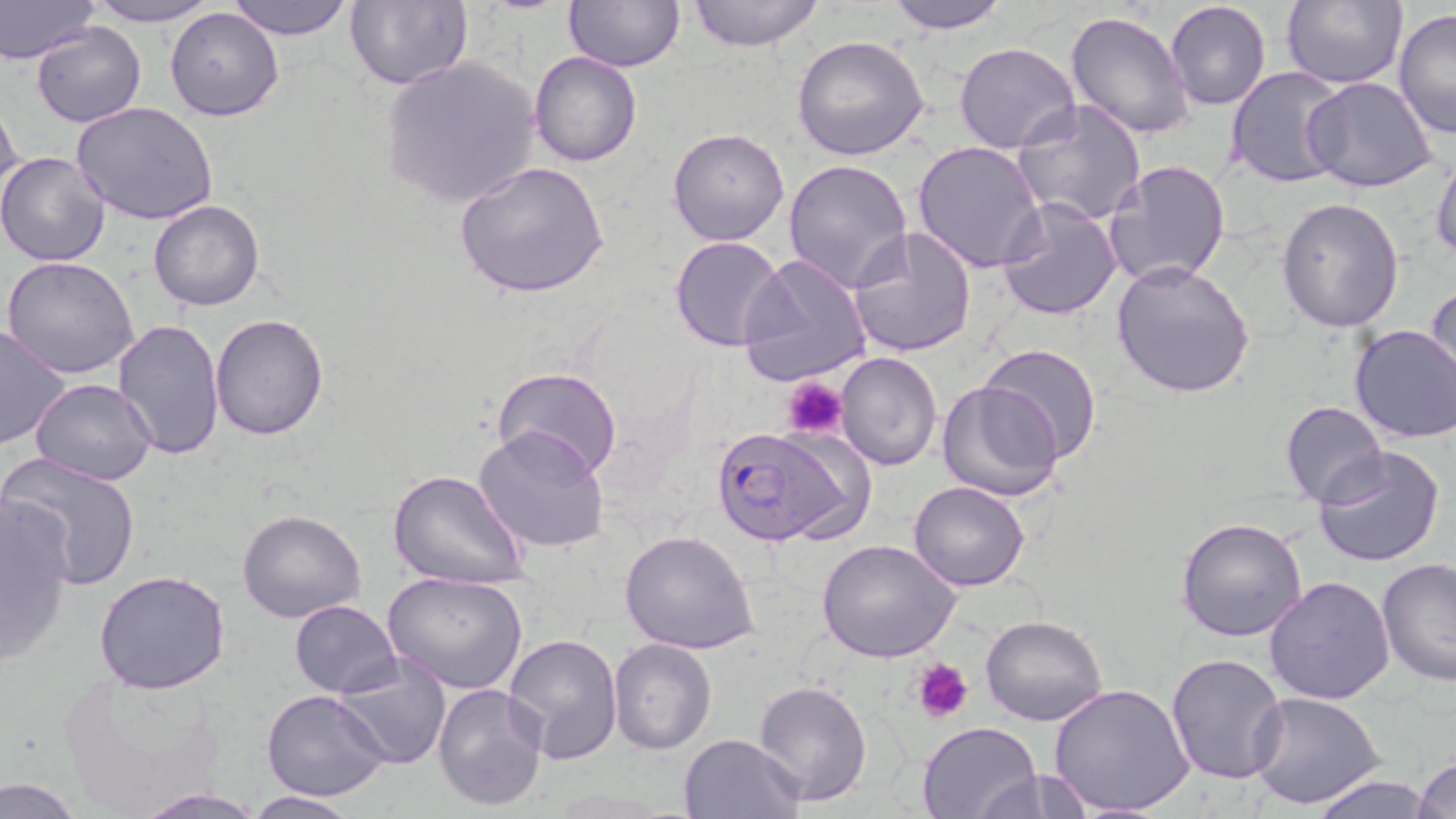

slide_level_diagnosis: Plasmodium falciparum
field_of_view: one of a larger specimen
stain: May-Grünwald-Giemsa
preparation: thin blood film
uninfected_red_blood_cell_locations: 'approximate bounding boxes as (x1,y1)-(x2,y2) corner pairs in pixels: (0,0)-(100,65), (81,0)-(224,26), (227,0)-(355,41), (347,0)-(473,90), (687,0)-(824,51), (886,0)-(1011,33), (1280,0)-(1407,91), (565,1)-(685,71), (1165,1)-(1271,110), (1393,7)-(1456,141), (165,8)-(284,122), (1065,9)-(1196,141), (32,23)-(147,127), (791,35)-(930,160), (952,41)-(1081,153), (530,52)-(643,167), (379,58)-(540,208), (1225,67)-(1350,188), (1302,76)-(1438,193), (0,94)-(23,208), (1013,100)-(1147,226), (73,102)-(221,225), (666,127)-(790,247), (913,139)-(1045,272), (0,150)-(111,268), (1431,150)-(1456,263), (783,156)-(914,293), (1103,158)-(1232,289), (452,161)-(610,299), (996,195)-(1123,320), (1275,198)-(1405,333), (149,199)-(265,312), (847,227)-(978,359), (669,236)-(785,353), (739,252)-(874,389), (2,255)-(140,378), (1112,260)-(1256,399), (1426,282)-(1456,393), (209,314)-(331,440), (111,319)-(227,460), (0,322)-(73,452), (1348,324)-(1456,444), (978,341)-(1102,465), (835,352)-(943,472), (491,366)-(621,482), (29,377)-(156,485), (937,378)-(1065,503), (1278,400)-(1388,508), (473,426)-(610,553), (1312,446)-(1445,569), (3,453)-(142,589), (386,468)-(532,592), (908,480)-(1029,592), (0,497)-(77,659), (236,509)-(365,624), (1177,517)-(1308,643), (619,529)-(760,654), (818,540)-(960,662), (1375,558)-(1456,687), (94,568)-(232,696), (382,571)-(528,694), (1264,575)-(1395,705), (289,599)-(402,697), (981,615)-(1106,726), (503,633)-(623,763), (610,639)-(715,753), (1166,652)-(1289,785), (334,657)-(452,769), (753,679)-(872,805), (431,682)-(549,812), (1049,682)-(1195,817), (262,690)-(392,802), (1249,693)-(1386,809), (915,721)-(1041,819), (679,733)-(804,819), (1412,754)-(1456,819), (969,766)-(1098,819), (1306,773)-(1436,818), (0,776)-(86,819), (135,788)-(267,818), (243,792)-(359,817)'
platelet_locations: 'approximate bounding boxes as (x1,y1)-(x2,y2) corner pairs in pixels: (781,374)-(847,441), (915,659)-(972,722)'
magnification: 1000x
image_size: 1456×819 pixels
modality: light microscopy
plasmodium_falciparum_infected_red_blood_cell_locations: 'approximate bounding boxes as (x1,y1)-(x2,y2) corner pairs in pixels: (708,423)-(865,547)'